Name the parasite shown.
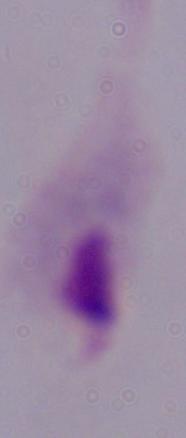

A trichomonad.

magnification: 1000x
modality: micrograph